Assess the morphology of the red blood cells.
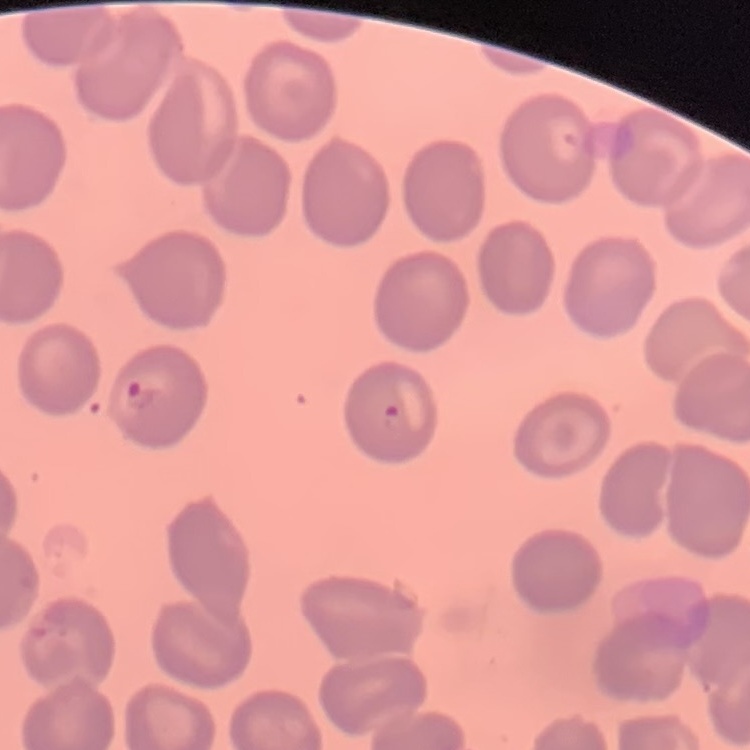
No rouleaux formation.

stain: Field's or Giemsa
preparation: thin blood smear
image_type: square crop of a larger photomicrograph